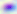 Captured at 400x magnification. Micrograph. Toxoplasma gondii is seen.